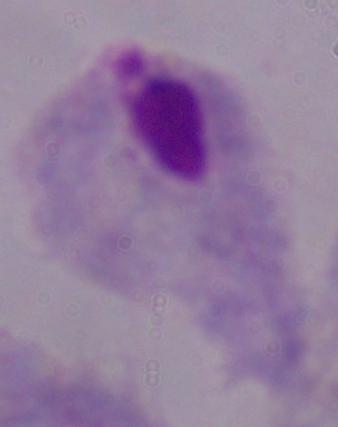
1000x magnification. A trichomonad is seen. Micrograph.